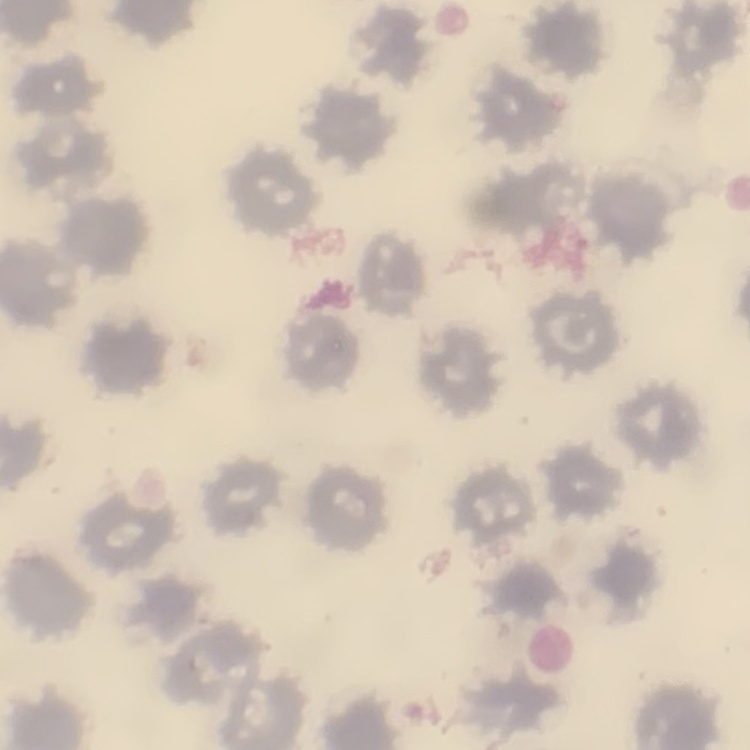
red_blood_cell_morphology: no rouleaux formation
stain: Field's or Giemsa
image_type: square crop of a larger photomicrograph
preparation: thin blood smear